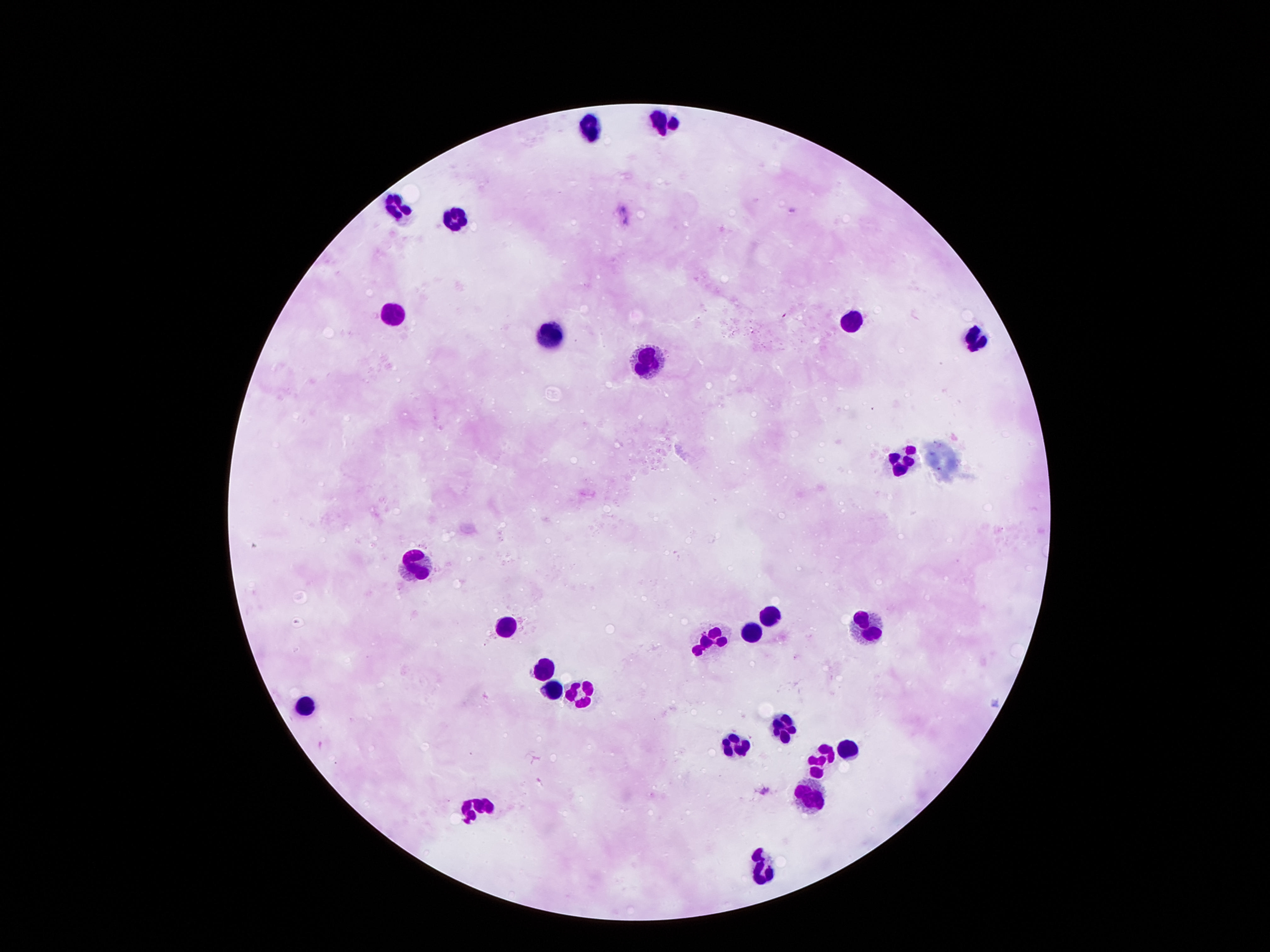 Approximate centers as (x, y) in pixels. Leukocyte locations: (664, 119), (594, 127), (390, 206), (448, 216), (388, 311), (849, 323), (554, 336), (975, 340), (642, 359), (898, 458), (416, 563), (771, 611), (866, 618), (502, 628), (751, 629), (713, 640), (543, 664), (554, 691), (582, 695), (307, 705), (781, 727), (825, 749), (848, 751), (736, 754), (812, 785), (479, 805), (761, 869). Thick peripheral-blood smear. 100x magnification. Image is 1270×952 pixels. One field from this slide. Smartphone photograph taken through the microscope eyepiece. Patient malaria status: uninfected. Giemsa stain.